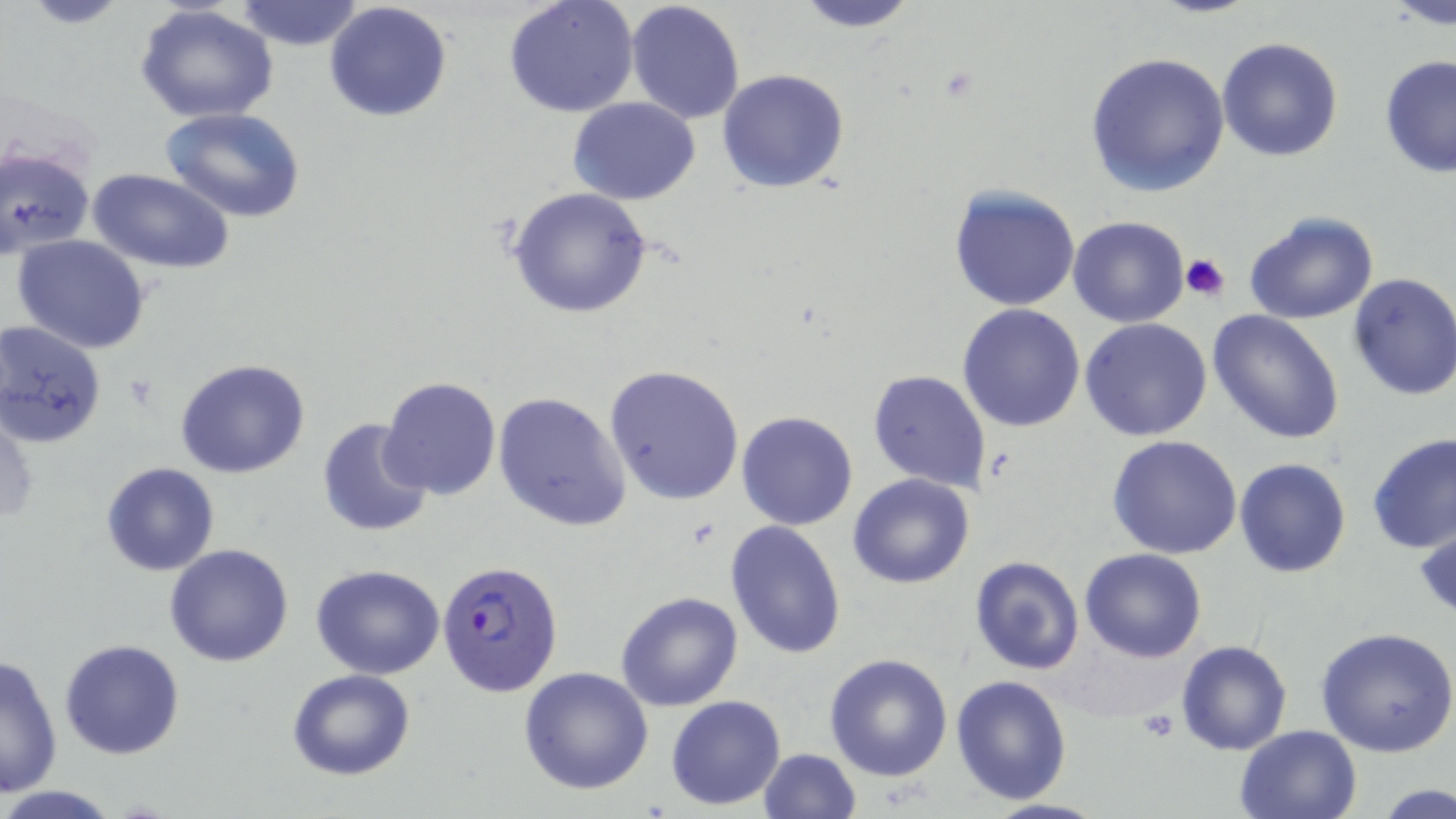
Approximate bounding boxes as [x1, y1, x2, y2] in pixels. Uninfected red blood cell locations: [18, 0, 136, 28], [236, 0, 364, 51], [504, 0, 639, 118], [626, 0, 745, 122], [787, 0, 922, 32], [324, 1, 452, 122], [1385, 1, 1455, 30], [134, 4, 279, 124], [1217, 36, 1343, 161], [1083, 51, 1230, 197], [1379, 53, 1456, 180], [718, 68, 850, 194], [569, 96, 699, 204], [160, 107, 305, 222], [1, 145, 96, 259], [90, 169, 233, 274], [946, 184, 1080, 311], [506, 186, 657, 320], [1243, 210, 1379, 325], [1067, 216, 1191, 328], [12, 234, 151, 353], [1346, 272, 1456, 400], [956, 303, 1088, 432], [1206, 308, 1347, 445], [1081, 318, 1213, 441], [1, 320, 107, 447], [175, 358, 312, 478], [605, 365, 746, 505], [867, 368, 991, 493], [378, 375, 503, 500], [493, 391, 631, 531], [0, 402, 37, 529], [736, 411, 858, 530], [316, 419, 434, 537], [1366, 433, 1456, 554], [1108, 435, 1242, 558], [1233, 458, 1351, 577], [100, 462, 220, 576], [847, 473, 976, 589], [1414, 512, 1456, 626], [724, 519, 847, 660], [164, 543, 294, 666], [1079, 548, 1206, 662], [969, 556, 1085, 674], [311, 565, 445, 680], [615, 591, 744, 711], [1315, 628, 1456, 758], [59, 638, 185, 759], [1174, 640, 1292, 755], [824, 651, 954, 781], [1, 654, 63, 796], [518, 666, 655, 795], [286, 669, 415, 780], [951, 674, 1073, 806], [665, 695, 785, 810], [1235, 724, 1361, 818], [757, 748, 862, 819], [1375, 782, 1455, 817], [0, 784, 123, 818], [980, 799, 1112, 819]. Platelet locations: [1180, 252, 1232, 300], [1138, 712, 1180, 741]. Plasmodium falciparum-infected red blood cell locations: [436, 559, 564, 697]. Slide-level diagnosis: Plasmodium falciparum. Image is 1456×819 pixels. 1000x magnification. Thin blood smear. Single field of view. Light microscopy. May-Grünwald-Giemsa stain.